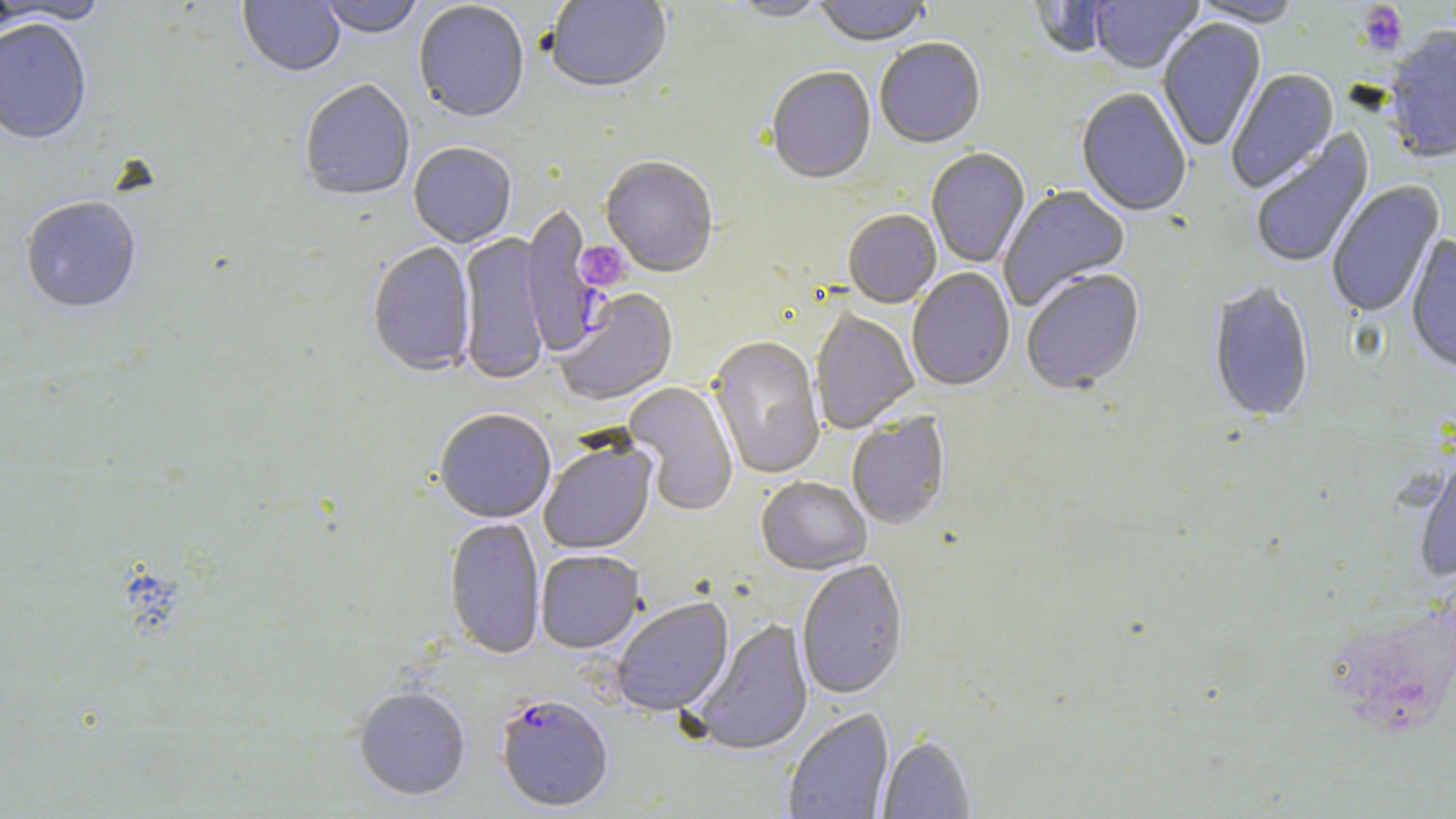

Summary:
  - Coordinate format: approximate bounding boxes as named x1/y1/x2/y2 corners in pixels
  - Plasmodium falciparum-infected red blood cell locations: (x1=519, y1=204, x2=603, y2=357), (x1=495, y1=695, x2=614, y2=813)
  - Platelet locations: (x1=1357, y1=3, x2=1407, y2=55), (x1=574, y1=240, x2=631, y2=292)
  - Uninfected red blood cell locations: (x1=238, y1=0, x2=345, y2=78), (x1=318, y1=0, x2=424, y2=41), (x1=545, y1=0, x2=672, y2=96), (x1=724, y1=0, x2=831, y2=24), (x1=813, y1=0, x2=931, y2=49), (x1=1089, y1=0, x2=1203, y2=76), (x1=1188, y1=0, x2=1304, y2=28), (x1=0, y1=1, x2=111, y2=26), (x1=1027, y1=1, x2=1114, y2=60), (x1=413, y1=2, x2=529, y2=125), (x1=0, y1=19, x2=92, y2=147), (x1=1157, y1=19, x2=1267, y2=152), (x1=1383, y1=27, x2=1456, y2=166), (x1=875, y1=40, x2=986, y2=150), (x1=766, y1=68, x2=876, y2=187), (x1=1226, y1=69, x2=1340, y2=195), (x1=300, y1=81, x2=415, y2=204), (x1=1076, y1=88, x2=1192, y2=219), (x1=1250, y1=130, x2=1375, y2=270), (x1=408, y1=144, x2=517, y2=249), (x1=926, y1=149, x2=1031, y2=269), (x1=601, y1=158, x2=717, y2=279), (x1=1327, y1=181, x2=1445, y2=318), (x1=999, y1=186, x2=1131, y2=311), (x1=20, y1=198, x2=142, y2=315), (x1=843, y1=211, x2=941, y2=310), (x1=458, y1=233, x2=550, y2=386), (x1=1405, y1=235, x2=1456, y2=376), (x1=367, y1=243, x2=476, y2=379), (x1=907, y1=269, x2=1015, y2=392), (x1=1022, y1=270, x2=1145, y2=397), (x1=1208, y1=283, x2=1314, y2=425), (x1=555, y1=289, x2=679, y2=407), (x1=810, y1=310, x2=919, y2=434), (x1=707, y1=337, x2=825, y2=480), (x1=624, y1=382, x2=739, y2=516), (x1=434, y1=410, x2=556, y2=524), (x1=847, y1=414, x2=951, y2=531), (x1=538, y1=438, x2=658, y2=555), (x1=1414, y1=453, x2=1456, y2=582), (x1=756, y1=477, x2=872, y2=577), (x1=444, y1=518, x2=546, y2=661), (x1=536, y1=551, x2=645, y2=654), (x1=796, y1=561, x2=909, y2=700), (x1=611, y1=598, x2=734, y2=717), (x1=690, y1=618, x2=814, y2=756), (x1=353, y1=687, x2=471, y2=802), (x1=783, y1=708, x2=894, y2=819), (x1=877, y1=736, x2=975, y2=818)
  - Slide-level diagnosis: Plasmodium falciparum
  - Magnification: 1000x
  - Preparation: thin blood film
  - Image size: 1456×819 pixels
  - Modality: light microscopy
  - Stain: May-Grünwald-Giemsa
  - Field of view: single